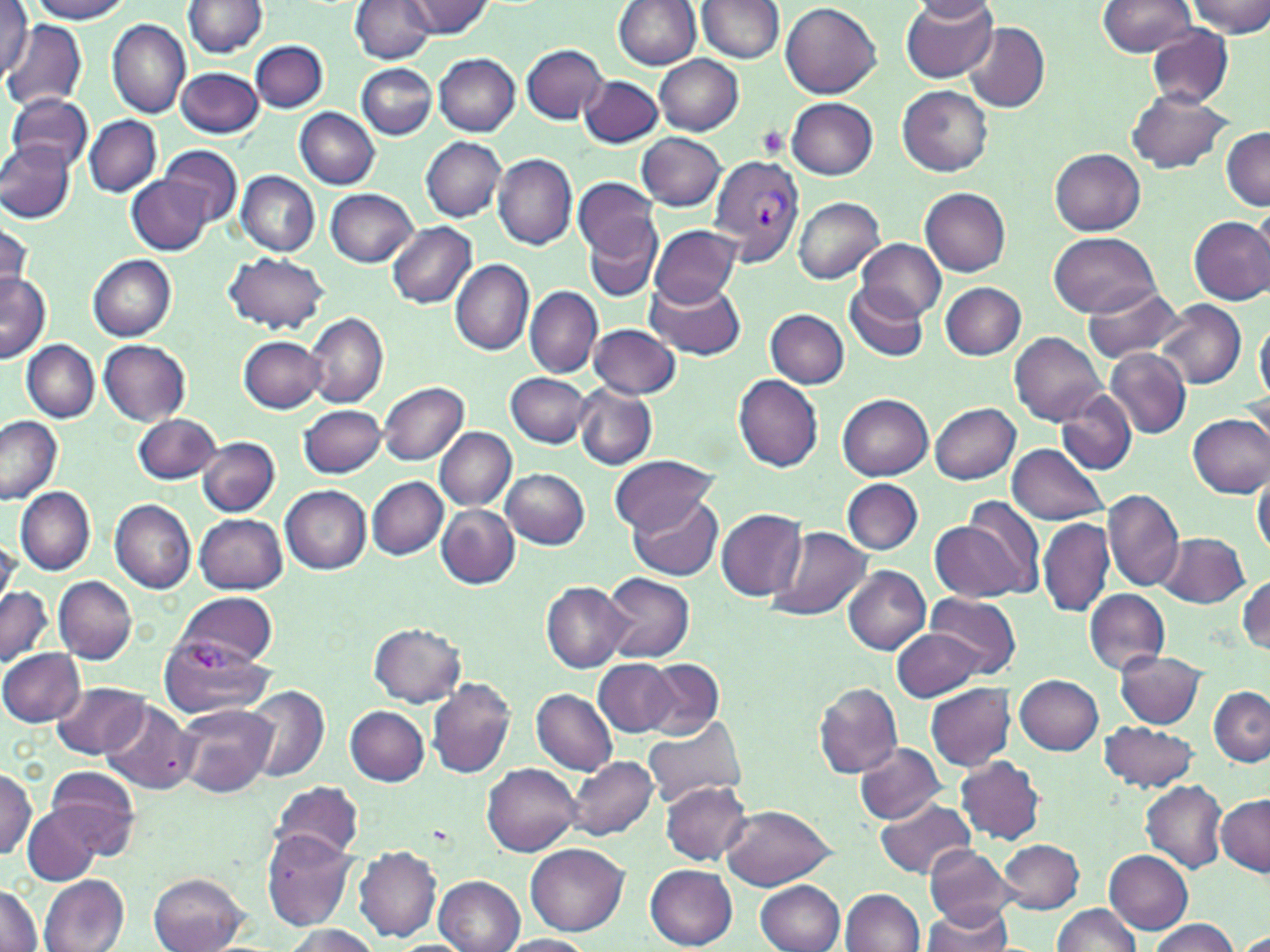
slide-level diagnosis = Plasmodium vivax
platelet locations = approximate bounding boxes as (x1,y1)-(x2,y2) corner pairs in pixels: (754,124)-(791,160)
preparation = thin blood film
magnification = 1000x
modality = light microscopy
stain = May-Grünwald-Giemsa
field of view = single
image size = 1270×952 pixels
Plasmodium vivax-infected red blood cell locations = approximate bounding boxes as (x1,y1)-(x2,y2) corner pairs in pixels: (709,154)-(806,267), (158,638)-(275,716)
uninfected red blood cell locations = approximate bounding boxes as (x1,y1)-(x2,y2) corner pairs in pixels: (30,0)-(133,24), (350,0)-(436,64), (404,0)-(492,40), (614,0)-(702,70), (900,0)-(997,83), (1096,0)-(1200,57), (1187,0)-(1270,38), (183,1)-(268,59), (696,1)-(784,64), (913,2)-(998,25), (782,3)-(883,100), (0,4)-(32,80), (107,19)-(189,118), (2,21)-(86,111), (963,21)-(1050,113), (1145,26)-(1234,108), (250,39)-(327,112), (521,44)-(608,124), (433,53)-(521,135), (655,55)-(744,136), (357,63)-(436,139), (177,67)-(263,138), (580,75)-(661,147), (898,85)-(993,177), (1124,89)-(1232,174), (7,92)-(92,175), (786,97)-(877,180), (296,107)-(380,190), (84,115)-(161,198), (1220,125)-(1269,210), (636,133)-(726,210), (421,137)-(507,222), (0,141)-(76,221), (159,146)-(242,228), (1050,148)-(1146,235), (493,152)-(578,250), (236,171)-(321,256), (129,177)-(210,256), (574,178)-(660,260), (919,187)-(1011,276), (326,188)-(417,267), (794,198)-(885,283), (1251,202)-(1270,278), (1188,215)-(1270,305), (584,216)-(661,304), (1,219)-(34,301), (387,222)-(476,308), (650,224)-(742,307), (1047,233)-(1162,318), (856,239)-(946,320), (224,252)-(329,335), (88,254)-(177,342), (450,259)-(533,355), (0,272)-(49,363), (646,280)-(747,358), (845,283)-(929,362), (941,283)-(1026,360), (524,285)-(602,378), (1080,287)-(1184,364), (763,297)-(930,377), (1155,300)-(1246,389), (765,308)-(848,387), (306,311)-(388,408), (1255,317)-(1270,404), (589,323)-(682,399), (1010,331)-(1107,425), (238,336)-(324,413), (99,339)-(191,424), (22,340)-(98,421), (1105,348)-(1192,438), (506,371)-(590,447), (731,374)-(824,472), (378,380)-(469,466), (573,382)-(657,470), (1055,392)-(1136,473), (837,393)-(933,480), (929,402)-(1021,484), (300,405)-(386,478), (133,413)-(222,485), (1188,413)-(1270,498), (0,418)-(63,504), (434,427)-(516,509), (197,437)-(279,515), (1007,443)-(1107,526), (609,453)-(719,535), (501,468)-(590,548), (1252,472)-(1270,558), (368,476)-(449,560), (842,478)-(924,555), (281,485)-(371,574), (15,487)-(95,574), (1102,488)-(1182,591), (629,493)-(722,580), (941,495)-(1044,600), (110,499)-(196,593), (437,505)-(520,588), (717,507)-(806,600), (195,514)-(287,593), (1038,518)-(1114,617), (765,526)-(873,621), (1156,532)-(1249,608), (842,565)-(931,654), (601,572)-(695,663), (1237,573)-(1269,657), (54,576)-(137,664), (541,581)-(633,672), (0,588)-(52,667), (1084,590)-(1169,675), (176,591)-(278,668), (925,593)-(1020,679), (368,623)-(467,707), (891,627)-(985,703), (0,648)-(86,727), (1113,649)-(1205,728), (595,659)-(678,737), (644,660)-(724,738), (1014,674)-(1103,753), (426,677)-(516,779), (55,681)-(150,760), (812,682)-(903,778), (925,684)-(1017,772), (245,686)-(328,782), (1207,687)-(1270,766), (532,688)-(619,775), (99,700)-(196,796), (175,704)-(276,798), (345,706)-(430,786), (642,715)-(749,807), (1099,721)-(1201,792), (855,742)-(948,823), (565,756)-(659,841), (956,756)-(1045,845), (484,763)-(581,857), (0,767)-(38,859), (44,767)-(141,855), (270,780)-(364,861), (661,780)-(752,864), (1141,780)-(1227,874), (1215,794)-(1269,876), (874,798)-(978,880), (718,804)-(836,889), (24,807)-(103,885), (261,830)-(357,929), (996,838)-(1084,914), (525,843)-(630,934), (923,845)-(1016,927), (352,846)-(442,942), (1106,850)-(1193,934), (425,864)-(606,945), (646,865)-(737,949), (148,873)-(248,952), (38,875)-(129,950), (435,875)-(524,951), (755,880)-(845,952), (0,883)-(44,950), (840,888)-(925,952), (919,902)-(1013,952), (1050,904)-(1143,952), (1146,919)-(1238,952), (281,925)-(380,952), (1238,932)-(1270,952), (496,934)-(598,952)